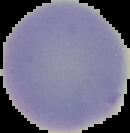

preparation = thin blood smear
image size = 130×133 pixels
malaria status = uninfected
image type = segmented cell region with the area outside set to black